Report the malaria status of this cell.
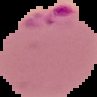
Parasitized.

{
  "image_type": "segmented cell region with the area outside set to black",
  "preparation": "thin blood smear",
  "image_size": "97×97 pixels"
}